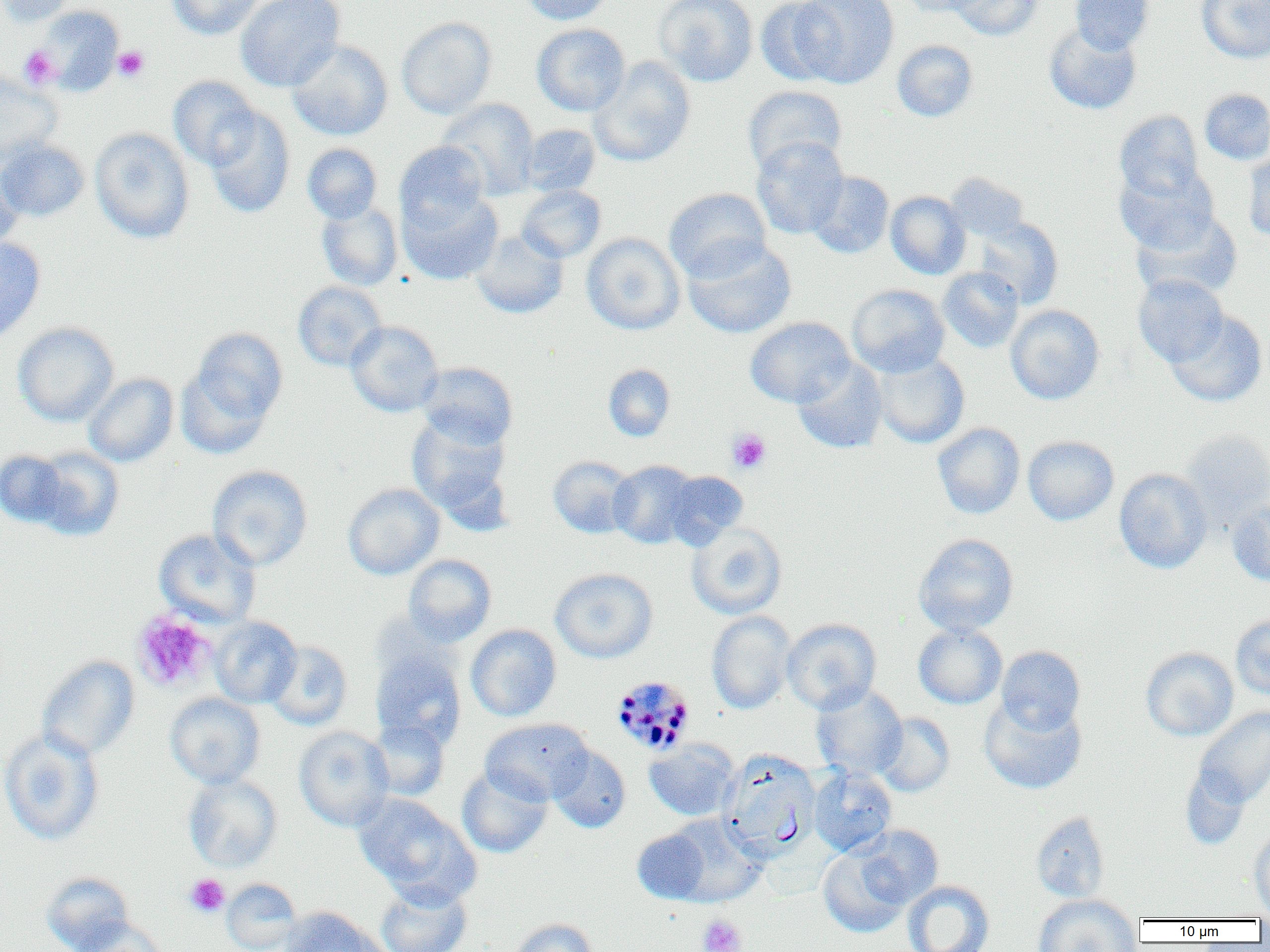

{
  "slide_level_diagnosis": "Plasmodium malariae",
  "uninfected_red_blood_cell_locations": "approximate bounding boxes as named x1/y1/x2/y2 corners in pixels: (x1=0, y1=0, x2=78, y2=27), (x1=167, y1=0, x2=265, y2=40), (x1=235, y1=0, x2=345, y2=92), (x1=519, y1=0, x2=615, y2=25), (x1=653, y1=0, x2=758, y2=87), (x1=755, y1=0, x2=844, y2=87), (x1=793, y1=0, x2=899, y2=88), (x1=898, y1=0, x2=986, y2=17), (x1=948, y1=0, x2=1042, y2=41), (x1=1070, y1=0, x2=1154, y2=54), (x1=1197, y1=0, x2=1270, y2=63), (x1=34, y1=5, x2=125, y2=96), (x1=396, y1=17, x2=497, y2=119), (x1=1044, y1=22, x2=1142, y2=115), (x1=532, y1=23, x2=631, y2=117), (x1=287, y1=39, x2=393, y2=140), (x1=892, y1=40, x2=978, y2=122), (x1=588, y1=56, x2=696, y2=167), (x1=0, y1=72, x2=62, y2=166), (x1=168, y1=75, x2=261, y2=170), (x1=743, y1=85, x2=847, y2=176), (x1=1200, y1=89, x2=1270, y2=165), (x1=437, y1=98, x2=540, y2=200), (x1=203, y1=107, x2=295, y2=219), (x1=1114, y1=110, x2=1204, y2=203), (x1=519, y1=123, x2=601, y2=197), (x1=89, y1=127, x2=195, y2=244), (x1=751, y1=136, x2=848, y2=239), (x1=0, y1=140, x2=90, y2=221), (x1=394, y1=141, x2=490, y2=231), (x1=301, y1=143, x2=383, y2=224), (x1=1242, y1=148, x2=1270, y2=242), (x1=0, y1=162, x2=23, y2=255), (x1=1115, y1=165, x2=1219, y2=253), (x1=807, y1=171, x2=894, y2=259), (x1=945, y1=172, x2=1031, y2=242), (x1=515, y1=184, x2=606, y2=262), (x1=663, y1=188, x2=771, y2=281), (x1=399, y1=189, x2=503, y2=285), (x1=885, y1=191, x2=971, y2=279), (x1=315, y1=200, x2=403, y2=291), (x1=1132, y1=209, x2=1242, y2=301), (x1=972, y1=217, x2=1063, y2=309), (x1=470, y1=229, x2=569, y2=319), (x1=581, y1=232, x2=685, y2=335), (x1=0, y1=236, x2=46, y2=344), (x1=682, y1=238, x2=797, y2=339), (x1=938, y1=266, x2=1024, y2=353), (x1=1133, y1=274, x2=1228, y2=367), (x1=293, y1=281, x2=387, y2=371), (x1=847, y1=284, x2=950, y2=377), (x1=1005, y1=304, x2=1105, y2=404), (x1=1165, y1=310, x2=1268, y2=407), (x1=745, y1=316, x2=854, y2=407), (x1=345, y1=320, x2=444, y2=417), (x1=13, y1=321, x2=119, y2=426), (x1=180, y1=326, x2=288, y2=449), (x1=870, y1=351, x2=969, y2=449), (x1=792, y1=358, x2=888, y2=454), (x1=417, y1=362, x2=518, y2=448), (x1=603, y1=364, x2=676, y2=442), (x1=84, y1=372, x2=179, y2=467), (x1=407, y1=412, x2=512, y2=524), (x1=932, y1=422, x2=1026, y2=519), (x1=1180, y1=428, x2=1270, y2=529), (x1=1022, y1=436, x2=1119, y2=525), (x1=28, y1=446, x2=125, y2=541), (x1=1, y1=448, x2=70, y2=529), (x1=548, y1=456, x2=637, y2=538), (x1=608, y1=460, x2=700, y2=548), (x1=207, y1=465, x2=313, y2=571), (x1=1114, y1=468, x2=1212, y2=573), (x1=663, y1=470, x2=748, y2=548), (x1=343, y1=482, x2=444, y2=579), (x1=1227, y1=497, x2=1270, y2=585), (x1=686, y1=523, x2=787, y2=620), (x1=153, y1=528, x2=261, y2=628), (x1=913, y1=533, x2=1018, y2=636), (x1=403, y1=554, x2=496, y2=646), (x1=549, y1=568, x2=658, y2=663), (x1=706, y1=611, x2=796, y2=714), (x1=1230, y1=615, x2=1270, y2=700), (x1=209, y1=616, x2=302, y2=708), (x1=782, y1=618, x2=881, y2=713), (x1=913, y1=623, x2=1007, y2=709), (x1=465, y1=624, x2=562, y2=721), (x1=265, y1=640, x2=353, y2=730), (x1=996, y1=645, x2=1085, y2=735), (x1=1140, y1=647, x2=1238, y2=741), (x1=370, y1=648, x2=466, y2=749), (x1=37, y1=655, x2=140, y2=761), (x1=810, y1=684, x2=908, y2=780), (x1=165, y1=692, x2=265, y2=789), (x1=980, y1=696, x2=1087, y2=794), (x1=1194, y1=706, x2=1270, y2=807), (x1=873, y1=712, x2=955, y2=796), (x1=480, y1=718, x2=594, y2=805), (x1=368, y1=720, x2=449, y2=801), (x1=294, y1=726, x2=395, y2=831), (x1=0, y1=728, x2=105, y2=847), (x1=644, y1=739, x2=740, y2=820), (x1=548, y1=744, x2=631, y2=833), (x1=720, y1=751, x2=820, y2=860), (x1=457, y1=766, x2=553, y2=858), (x1=809, y1=767, x2=897, y2=856), (x1=1180, y1=767, x2=1252, y2=850), (x1=183, y1=773, x2=283, y2=872), (x1=352, y1=793, x2=477, y2=902), (x1=1031, y1=811, x2=1110, y2=903), (x1=665, y1=814, x2=765, y2=907), (x1=855, y1=825, x2=943, y2=908), (x1=632, y1=828, x2=710, y2=903), (x1=1249, y1=828, x2=1270, y2=916), (x1=818, y1=846, x2=909, y2=937), (x1=41, y1=871, x2=133, y2=951), (x1=221, y1=878, x2=303, y2=952), (x1=902, y1=880, x2=994, y2=952), (x1=375, y1=881, x2=472, y2=952), (x1=1032, y1=894, x2=1141, y2=952), (x1=279, y1=907, x2=390, y2=952), (x1=70, y1=917, x2=167, y2=952), (x1=508, y1=918, x2=600, y2=952)",
  "preparation": "thin blood film",
  "field_of_view": "one of a larger specimen",
  "platelet_locations": "approximate bounding boxes as named x1/y1/x2/y2 corners in pixels: (x1=112, y1=46, x2=149, y2=81), (x1=19, y1=47, x2=59, y2=90), (x1=727, y1=428, x2=771, y2=474), (x1=132, y1=611, x2=216, y2=691), (x1=184, y1=874, x2=230, y2=917), (x1=697, y1=914, x2=746, y2=952)",
  "magnification": "1000x",
  "modality": "optical microscopy",
  "plasmodium_malariae_infected_red_blood_cell_locations": "approximate bounding boxes as named x1/y1/x2/y2 corners in pixels: (x1=610, y1=676, x2=695, y2=755)",
  "image_size": "1270×952 pixels"
}